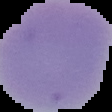
Summary:
  - Image type: segmented cell region with the area outside set to black
  - Preparation: thin blood film
  - Image size: 112×112 pixels
  - Malaria status: uninfected